Comment on the morphology of the red blood cells.
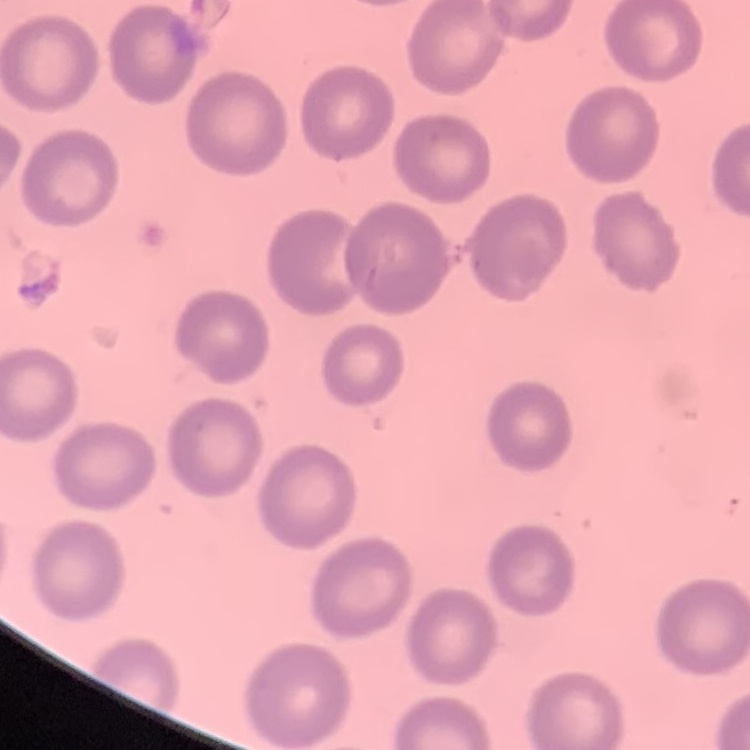
No rouleaux formation.

{
  "stain": "Field's or Giemsa",
  "image_type": "one tile cut from a larger photomicrograph",
  "preparation": "thin blood smear"
}